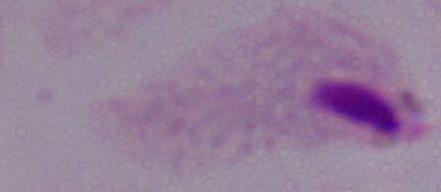
A trichomonad is seen. Micrograph. 1000x magnification.